Name the blood parasite species.
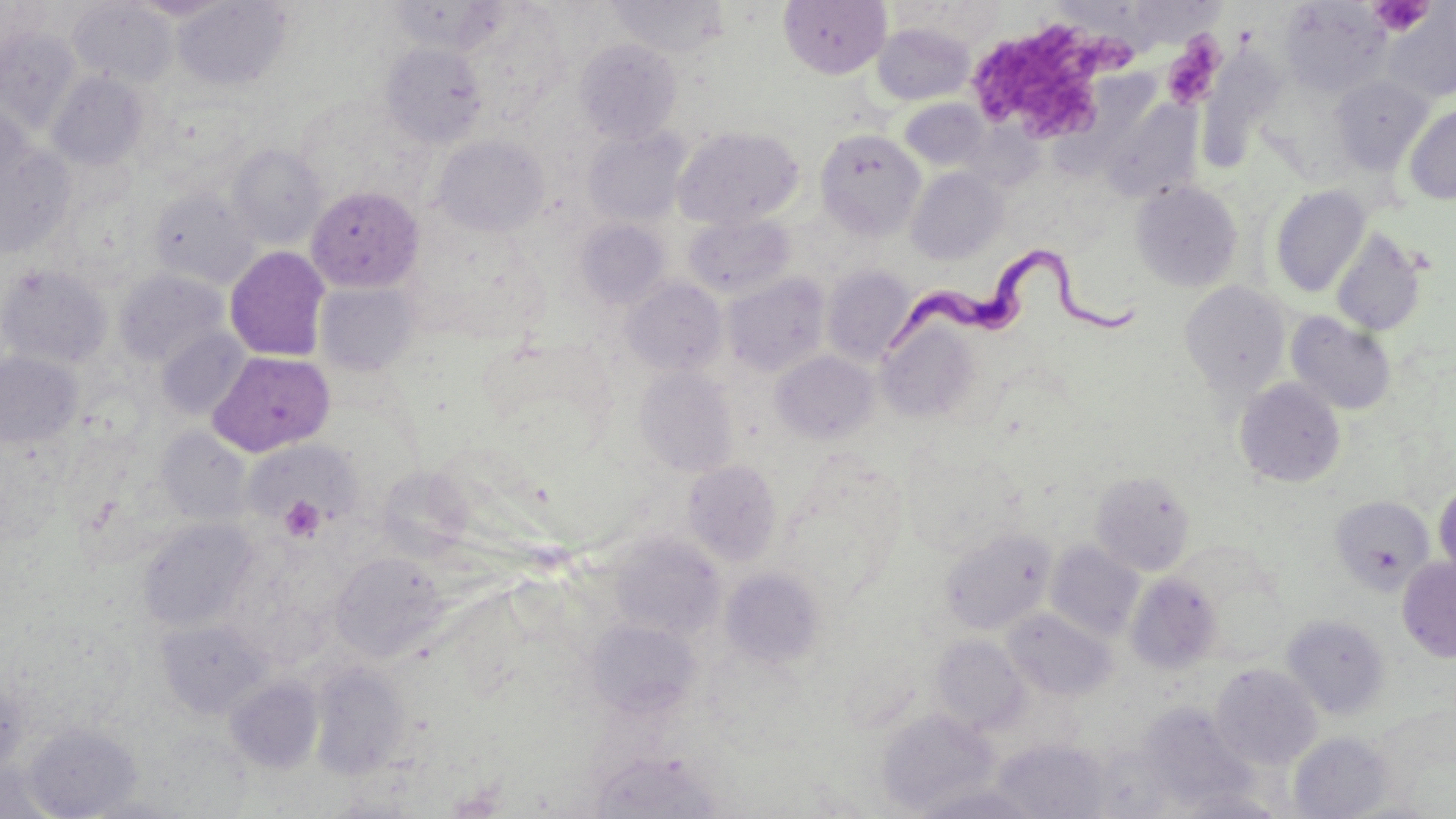
Trypanosoma brucei.

Approximate bounding boxes as named x1/y1/x2/y2 corners in pixels. Uninfected red blood cell locations: (x1=0, y1=0, x2=50, y2=72), (x1=127, y1=0, x2=234, y2=21), (x1=607, y1=0, x2=729, y2=58), (x1=778, y1=0, x2=891, y2=79), (x1=68, y1=1, x2=177, y2=87), (x1=173, y1=1, x2=292, y2=90), (x1=386, y1=1, x2=512, y2=57), (x1=890, y1=2, x2=1004, y2=53), (x1=1281, y1=2, x2=1390, y2=97), (x1=1383, y1=6, x2=1455, y2=104), (x1=872, y1=21, x2=976, y2=105), (x1=0, y1=26, x2=82, y2=134), (x1=575, y1=38, x2=682, y2=144), (x1=380, y1=42, x2=488, y2=148), (x1=1205, y1=45, x2=1279, y2=180), (x1=47, y1=71, x2=150, y2=170), (x1=1330, y1=75, x2=1432, y2=174), (x1=1100, y1=97, x2=1201, y2=202), (x1=899, y1=98, x2=991, y2=172), (x1=0, y1=99, x2=32, y2=194), (x1=1404, y1=102, x2=1456, y2=205), (x1=673, y1=126, x2=804, y2=229), (x1=583, y1=128, x2=689, y2=226), (x1=815, y1=128, x2=925, y2=240), (x1=432, y1=136, x2=549, y2=237), (x1=228, y1=144, x2=327, y2=248), (x1=0, y1=145, x2=76, y2=258), (x1=906, y1=167, x2=1006, y2=264), (x1=1131, y1=181, x2=1243, y2=292), (x1=306, y1=185, x2=425, y2=293), (x1=1270, y1=185, x2=1370, y2=298), (x1=148, y1=187, x2=259, y2=288), (x1=684, y1=214, x2=795, y2=299), (x1=575, y1=219, x2=670, y2=309), (x1=1331, y1=228, x2=1427, y2=337), (x1=224, y1=246, x2=331, y2=362), (x1=0, y1=265, x2=112, y2=369), (x1=821, y1=265, x2=915, y2=365), (x1=115, y1=269, x2=227, y2=368), (x1=722, y1=274, x2=831, y2=377), (x1=622, y1=278, x2=728, y2=376), (x1=1179, y1=281, x2=1291, y2=399), (x1=315, y1=282, x2=420, y2=376), (x1=1286, y1=312, x2=1397, y2=415), (x1=876, y1=320, x2=985, y2=424), (x1=156, y1=328, x2=251, y2=419), (x1=770, y1=350, x2=879, y2=445), (x1=0, y1=351, x2=82, y2=449), (x1=209, y1=351, x2=336, y2=457), (x1=634, y1=365, x2=739, y2=478), (x1=1234, y1=377, x2=1346, y2=488), (x1=156, y1=427, x2=253, y2=525), (x1=241, y1=437, x2=362, y2=531), (x1=0, y1=439, x2=64, y2=548), (x1=899, y1=445, x2=1023, y2=559), (x1=683, y1=459, x2=782, y2=566), (x1=376, y1=466, x2=473, y2=561), (x1=1090, y1=470, x2=1195, y2=576), (x1=1433, y1=479, x2=1456, y2=582), (x1=1330, y1=495, x2=1435, y2=595), (x1=138, y1=518, x2=257, y2=632), (x1=939, y1=528, x2=1056, y2=635), (x1=610, y1=533, x2=726, y2=640), (x1=1046, y1=540, x2=1145, y2=641), (x1=331, y1=552, x2=446, y2=661), (x1=1397, y1=556, x2=1456, y2=662), (x1=720, y1=567, x2=829, y2=670), (x1=1125, y1=572, x2=1222, y2=675), (x1=1003, y1=608, x2=1116, y2=701), (x1=1282, y1=614, x2=1390, y2=719), (x1=156, y1=617, x2=273, y2=718), (x1=585, y1=619, x2=700, y2=719), (x1=931, y1=635, x2=1029, y2=734), (x1=309, y1=662, x2=411, y2=779), (x1=1211, y1=663, x2=1321, y2=770), (x1=226, y1=676, x2=323, y2=773), (x1=0, y1=680, x2=29, y2=777), (x1=1138, y1=704, x2=1262, y2=810), (x1=877, y1=709, x2=998, y2=815), (x1=24, y1=724, x2=142, y2=818), (x1=1289, y1=731, x2=1395, y2=819), (x1=992, y1=740, x2=1111, y2=817), (x1=589, y1=749, x2=720, y2=818), (x1=2, y1=763, x2=62, y2=818), (x1=912, y1=782, x2=1043, y2=819), (x1=1168, y1=787, x2=1290, y2=818), (x1=79, y1=793, x2=193, y2=818), (x1=1336, y1=797, x2=1447, y2=818). Trypanosoma brucei locations: (x1=882, y1=249, x2=1140, y2=353). Platelet locations: (x1=1371, y1=0, x2=1432, y2=36), (x1=977, y1=21, x2=1136, y2=137), (x1=1162, y1=38, x2=1222, y2=109), (x1=279, y1=495, x2=326, y2=542). May-Grünwald-Giemsa-stained preparation. 1000x magnification. Thin blood film. Light microscopy. Single field of view. Image is 1456×819 pixels.